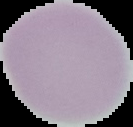 Result: no malaria parasites seen. Segmented cell region on a black background. Image is 133×127 pixels. From a thin blood smear.